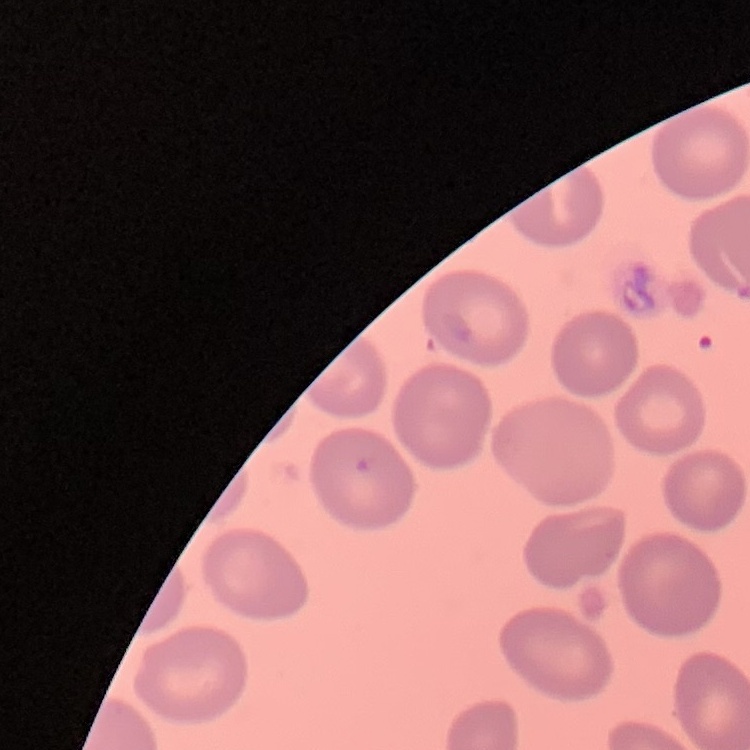

red blood cell morphology = no rouleaux formation
stain = Field's or Giemsa
image type = square crop of a larger photomicrograph
preparation = thin blood smear